Name the parasite shown.
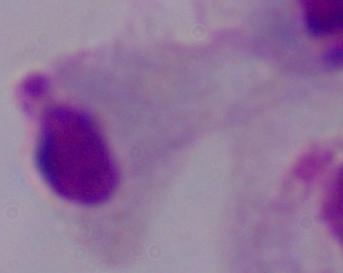
This is a trichomonad.

modality = micrograph
magnification = 1000x